Evaluate for Plasmodium parasites.
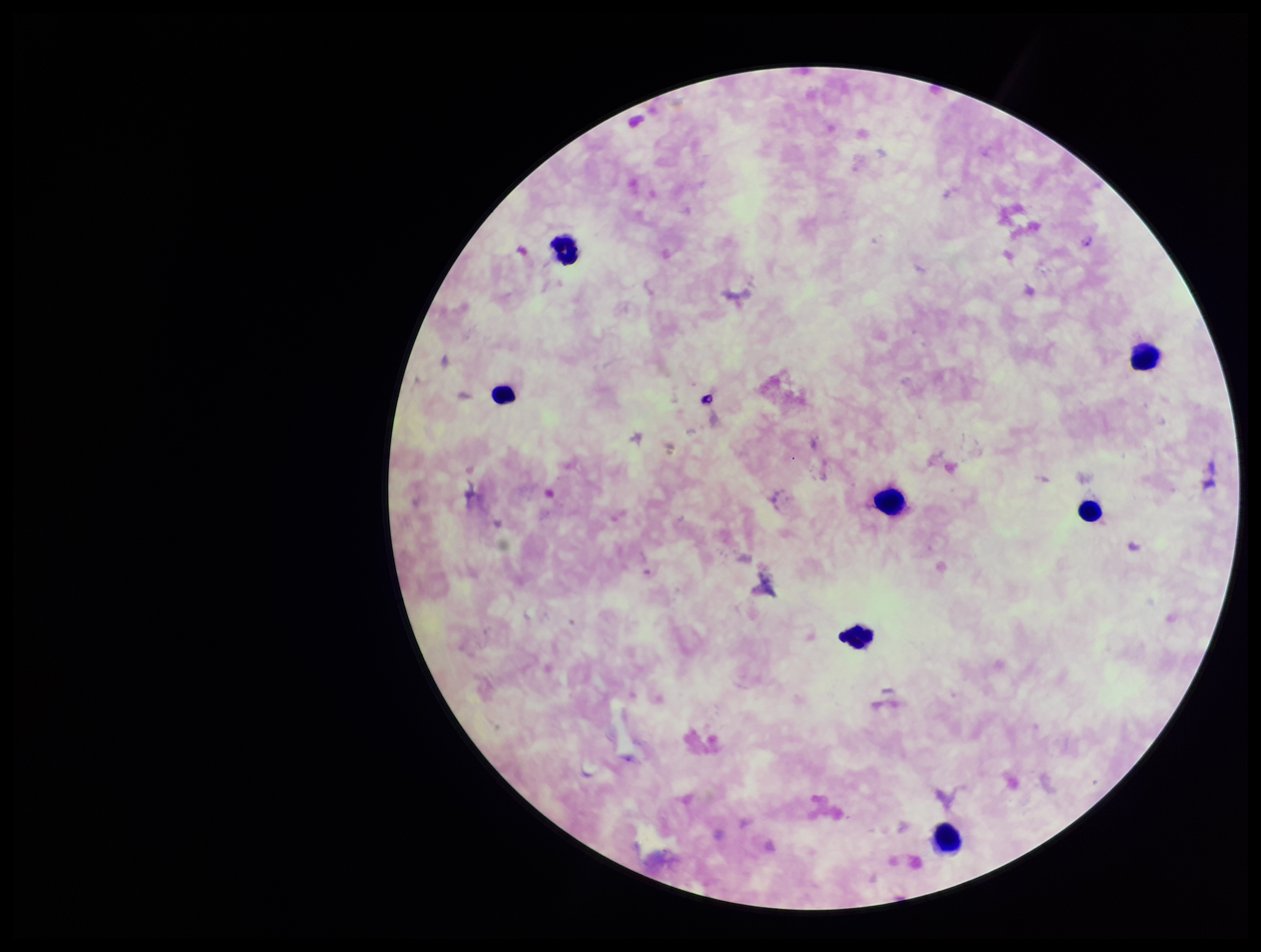

Detected.

Giemsa stain. Image is 1261×952 pixels. Photographed through the microscope eyepiece with a smartphone camera. Species reported for this patient: Plasmodium falciparum. Leukocyte count: 7. Preparation: thick. Parasite count: 1. Single field of view. Patient malaria status: positive.